Give the extent of all Plasmodium malariae-infected red blood cells.
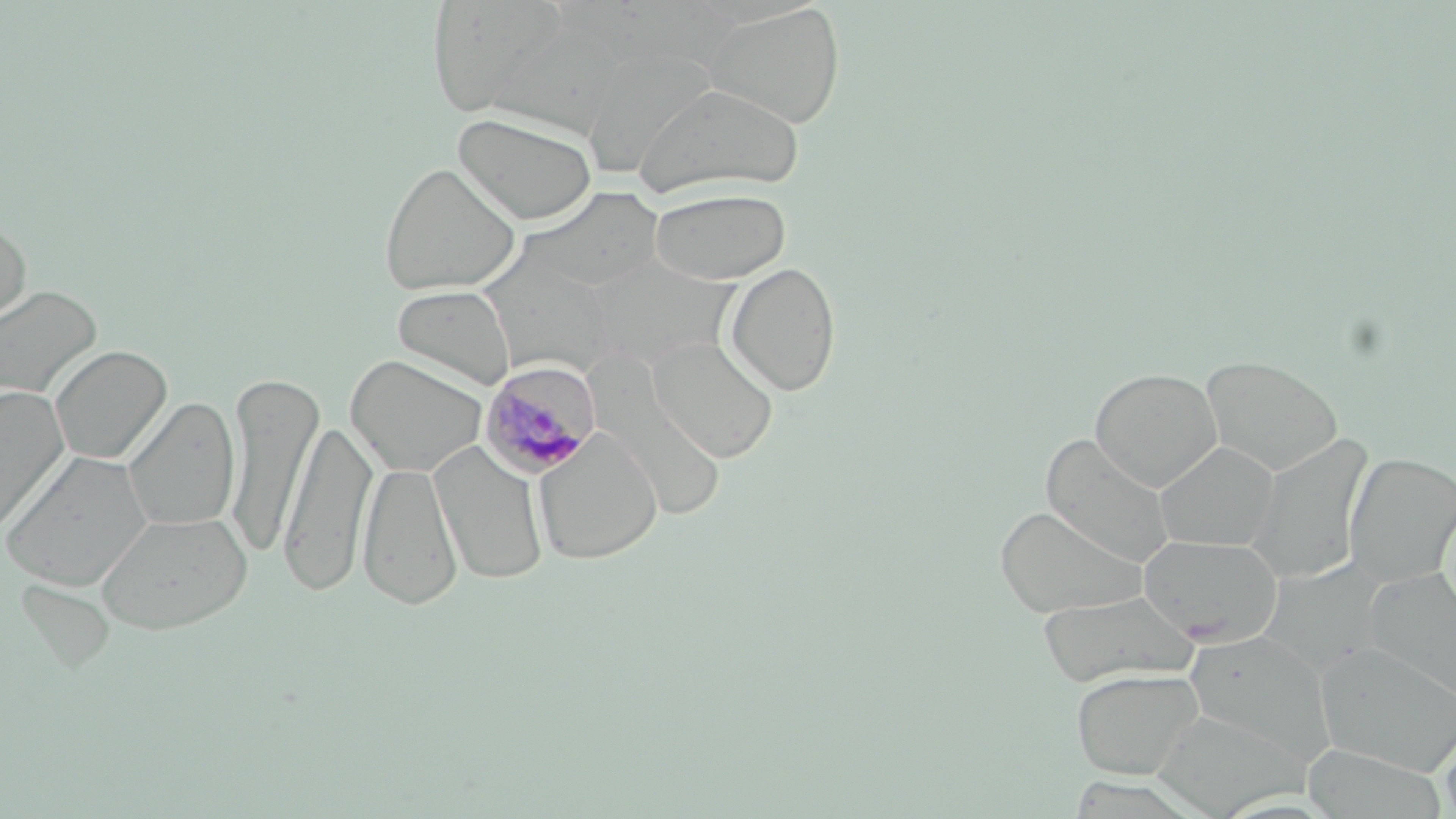
Approximate bounding boxes as [x1, y1, x2, y2] in pixels.
Plasmodium malariae-infected red blood cells: [478, 360, 601, 479].

Summary:
  - Uninfected red blood cell locations: [424, 0, 577, 120], [702, 3, 846, 129], [578, 43, 720, 177], [634, 81, 805, 199], [453, 110, 598, 225], [378, 161, 520, 297], [515, 187, 666, 297], [648, 187, 792, 285], [0, 216, 32, 329], [478, 255, 619, 378], [724, 262, 841, 396], [392, 284, 516, 390], [0, 285, 102, 401], [648, 336, 779, 463], [49, 345, 172, 466], [345, 354, 488, 477], [1201, 354, 1344, 476], [586, 358, 727, 523], [1090, 368, 1223, 491], [224, 372, 325, 558], [0, 385, 70, 535], [123, 396, 240, 532], [279, 418, 377, 598], [533, 430, 663, 566], [1040, 435, 1175, 566], [1245, 436, 1372, 585], [428, 440, 551, 586], [1156, 441, 1279, 550], [2, 451, 155, 591], [1344, 452, 1456, 586], [358, 460, 463, 611], [994, 505, 1148, 619], [96, 510, 253, 635], [1138, 535, 1283, 642], [1361, 569, 1456, 705], [15, 578, 116, 673], [1037, 591, 1197, 686], [1314, 642, 1456, 776], [1071, 668, 1205, 780], [1150, 707, 1308, 817], [1439, 719, 1456, 819], [1301, 744, 1448, 818]
  - Slide-level diagnosis: Plasmodium malariae
  - Stain: May-Grünwald-Giemsa
  - Preparation: thin blood smear
  - Modality: light microscopy
  - Magnification: 1000x
  - Field of view: one of a larger specimen
  - Image size: 1456×819 pixels